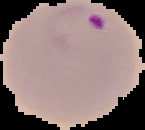
From a thin blood smear. Cell region segmented out of the field of view; the surrounding area is masked to black. Image is 145×130 pixels. Result: Plasmodium parasites detected.